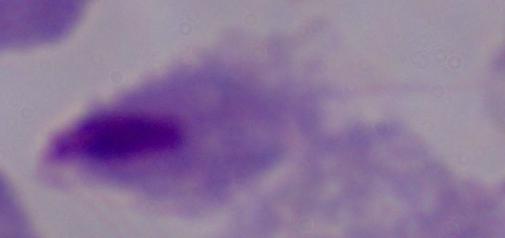
Photomicrograph. A trichomonad is seen. Captured at 1000x magnification.